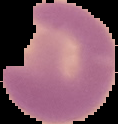

preparation = thin blood film
image type = segmented cell region with the area outside set to black
image size = 118×124 pixels
result = malaria parasites identified